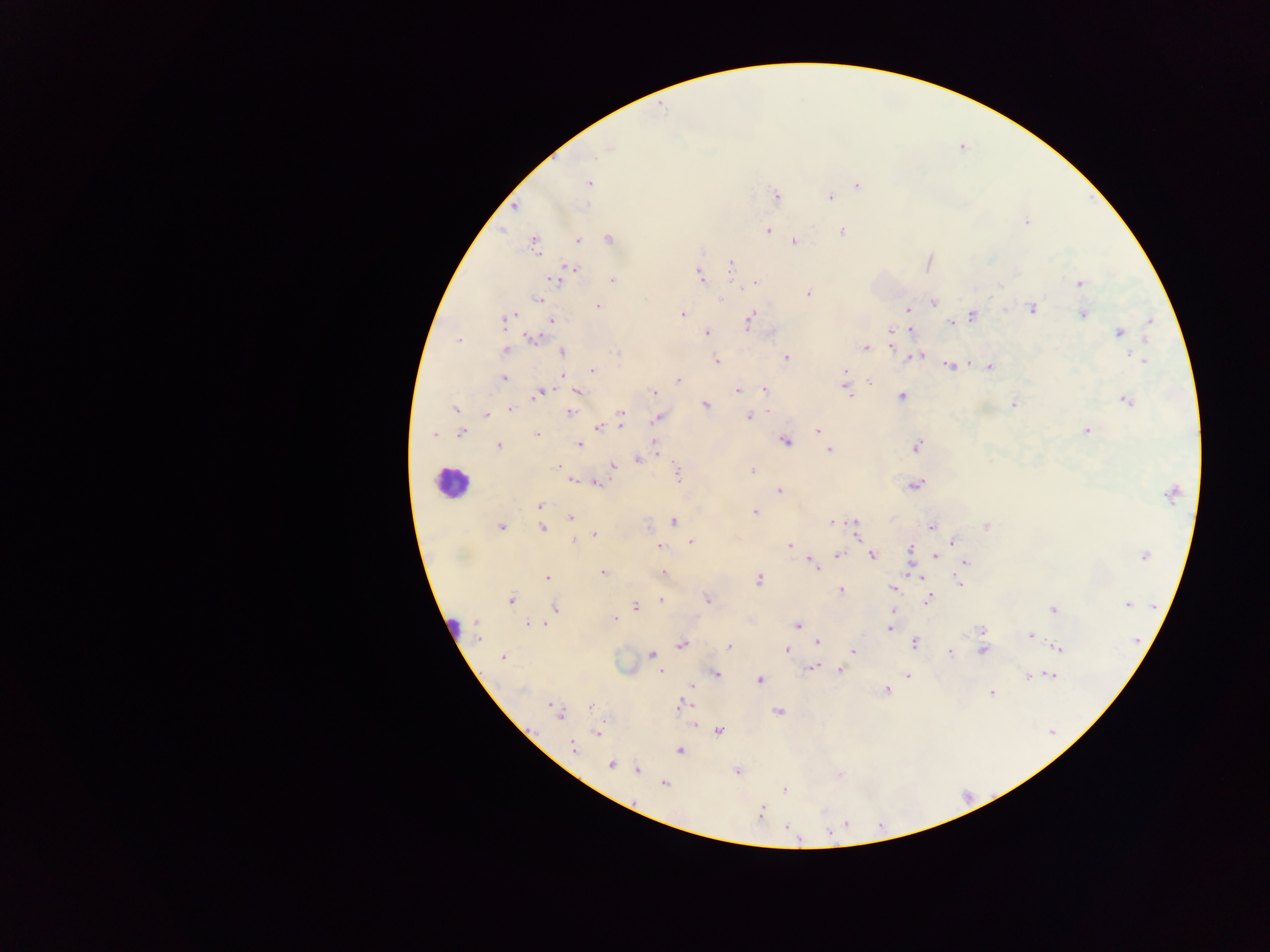
Approximate centers as {x, y} in pixels.
Summary:
  - Leukocyte locations (subset; some below the resolvable size): {449, 482}, {453, 628}
  - Malaria parasite locations: {609, 148}, {589, 183}, {858, 185}, {777, 196}, {830, 197}, {515, 206}, {1026, 222}, {767, 230}, {842, 232}, {610, 239}, {578, 240}, {795, 242}, {533, 245}, {731, 264}, {571, 270}, {559, 275}, {700, 275}, {612, 280}, {756, 283}, {1078, 284}, {998, 286}, {808, 293}, {537, 301}, {933, 303}, {598, 307}, {908, 309}, {1032, 309}, {683, 314}, {1083, 314}, {973, 316}, {504, 320}, {552, 320}, {750, 320}, {952, 322}, {1150, 322}, {892, 330}, {909, 331}, {1119, 332}, {707, 333}, {534, 338}, {458, 340}, {891, 345}, {865, 348}, {505, 350}, {618, 351}, {562, 352}, {919, 356}, {786, 357}, {1143, 360}, {716, 361}, {950, 366}, {990, 366}, {592, 370}, {844, 372}, {504, 379}, {678, 380}, {843, 380}, {870, 382}, {846, 388}, {765, 389}, {738, 390}, {576, 391}, {541, 392}, {654, 393}, {902, 396}, {1126, 400}, {1014, 404}, {704, 405}, {455, 409}, {511, 409}, {570, 412}, {621, 413}, {486, 414}, {749, 416}, {658, 418}, {621, 424}, {598, 428}, {818, 429}, {1086, 431}, {461, 433}, {434, 434}, {537, 434}, {785, 441}, {579, 445}, {498, 446}, {917, 446}, {656, 447}, {829, 450}, {639, 459}, {558, 466}, {613, 466}, {752, 471}, {678, 473}, {572, 480}, {598, 484}, {915, 484}, {779, 490}, {1172, 494}, {540, 506}, {755, 513}, {570, 517}, {674, 521}, {833, 523}, {854, 524}, {931, 526}, {986, 526}, {502, 527}, {543, 528}, {856, 530}, {595, 535}, {574, 542}, {691, 542}, {954, 542}, {790, 545}, {659, 546}, {910, 549}, {838, 554}, {872, 556}, {1144, 556}, {936, 557}, {966, 562}, {812, 563}, {603, 573}, {664, 573}, {920, 576}, {547, 577}, {759, 580}, {958, 582}, {893, 588}, {841, 590}, {708, 599}, {928, 600}, {511, 601}, {661, 601}, {1128, 604}, {636, 607}, {555, 609}, {1054, 609}, {614, 618}, {528, 623}, {539, 624}, {476, 625}, {797, 626}, {890, 628}, {981, 629}, {1030, 635}, {478, 638}, {817, 642}, {914, 643}, {681, 644}, {729, 647}, {1060, 648}, {786, 651}, {982, 651}, {853, 652}, {950, 653}, {652, 655}, {502, 657}, {810, 668}, {660, 671}, {839, 671}, {715, 674}, {1052, 675}, {907, 676}, {1027, 676}, {759, 681}, {692, 685}, {522, 690}, {886, 690}, {992, 693}, {552, 705}, {680, 705}, {591, 706}, {778, 712}, {558, 714}, {719, 731}, {597, 734}, {572, 747}, {679, 750}, {611, 764}, {638, 770}, {737, 771}, {839, 776}, {665, 784}, {785, 790}, {761, 813}, {847, 824}, {788, 826}, {830, 833}
  - Image size: 1270×952 pixels
  - Field of view: single
  - Capture: mobile-phone photograph through a microscope
  - Country: Ghana
  - Preparation: thick blood smear